State which cell type is depicted.
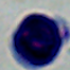
This is a leukocyte.

modality = photomicrograph
magnification = 1000x